Locate and identify every blood parasite.
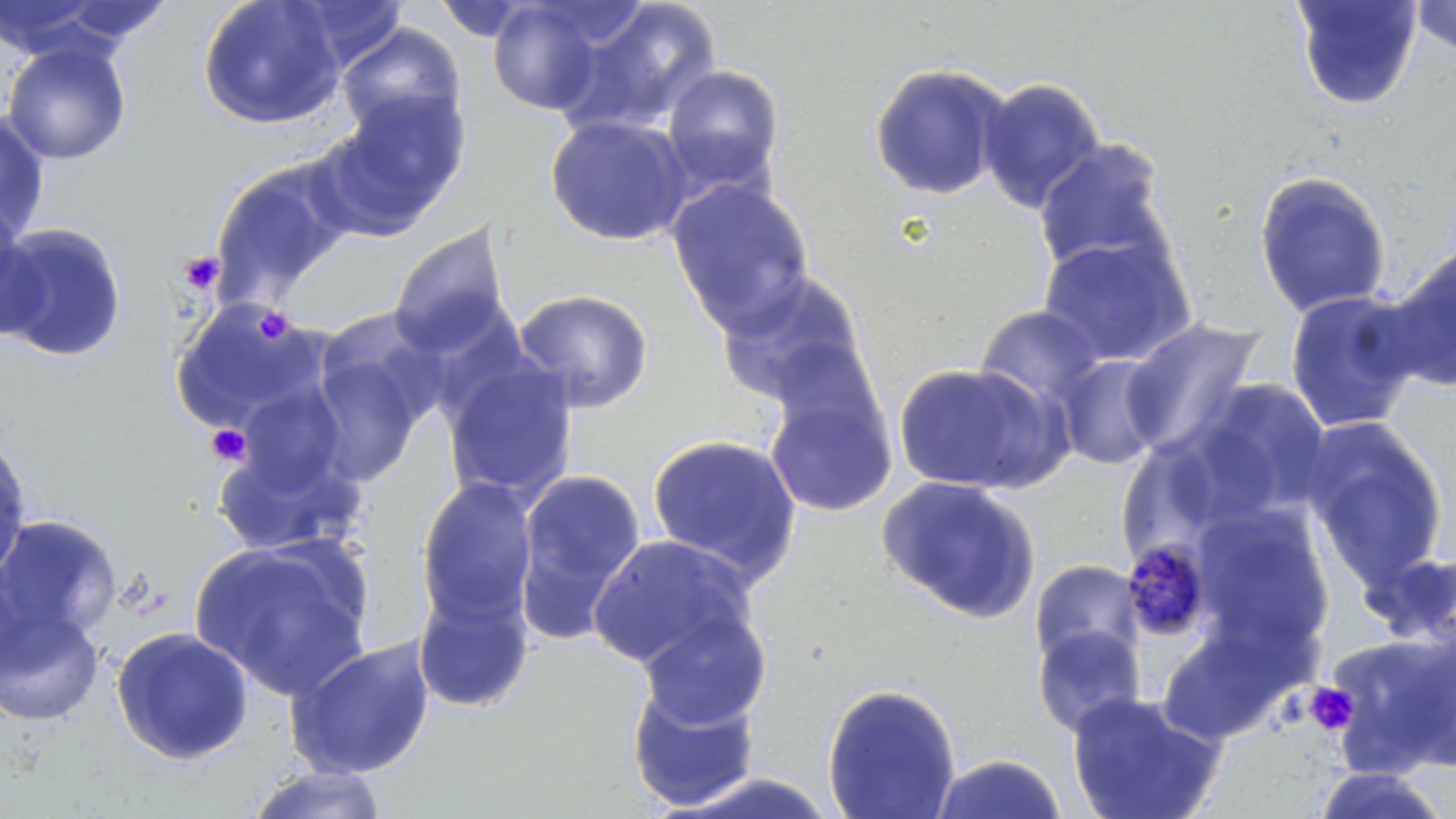
Approximate bounding boxes as [x1, y1, x2, y2] in pixels.
Plasmodium malariae-infected red blood cells: [1118, 533, 1212, 638].
No Plasmodium falciparum, Plasmodium ovale, Plasmodium vivax, Babesia divergens, or Trypanosoma brucei observed.

slide_level_diagnosis: Plasmodium malariae
platelet_locations: 'approximate bounding boxes as [x1, y1, x2, y2] in pixels: [177, 250, 225, 295], [253, 305, 294, 343], [206, 423, 252, 467], [1303, 682, 1359, 736]'
magnification: 1000x
image_size: 1456×819 pixels
preparation: thin blood film
modality: light microscopy
field_of_view: one of a larger specimen
stain: May-Grünwald-Giemsa
uninfected_red_blood_cell_locations: 'approximate bounding boxes as [x1, y1, x2, y2] in pixels: [0, 0, 161, 61], [196, 0, 346, 130], [282, 0, 411, 71], [485, 0, 615, 117], [1409, 0, 1456, 59], [429, 1, 546, 43], [562, 1, 721, 133], [1290, 1, 1423, 111], [336, 22, 467, 141], [1, 40, 132, 165], [868, 62, 1013, 202], [661, 64, 785, 195], [978, 76, 1106, 214], [312, 94, 470, 240], [0, 110, 51, 243], [545, 114, 693, 247], [1033, 138, 1173, 278], [209, 156, 358, 307], [1252, 169, 1392, 319], [665, 177, 816, 334], [0, 205, 44, 342], [1, 222, 128, 363], [387, 222, 515, 359], [1037, 235, 1197, 368], [1380, 244, 1455, 392], [715, 269, 872, 412], [512, 288, 654, 414], [1283, 289, 1423, 434], [169, 297, 327, 434], [975, 304, 1106, 411], [1120, 318, 1267, 460], [308, 333, 432, 488], [1055, 355, 1168, 471], [442, 360, 578, 504], [891, 361, 1064, 495], [1179, 378, 1334, 526], [233, 380, 353, 499], [764, 381, 897, 519], [1301, 417, 1448, 585], [0, 431, 33, 588], [645, 433, 803, 585], [212, 435, 364, 557], [1123, 439, 1212, 558], [513, 469, 647, 641], [877, 475, 1042, 623], [415, 478, 539, 629], [1191, 503, 1336, 656], [0, 514, 121, 642], [586, 534, 758, 675], [188, 537, 374, 701], [1361, 548, 1456, 659], [1029, 559, 1144, 669], [413, 584, 535, 713], [0, 600, 105, 728], [634, 608, 773, 731], [1156, 618, 1306, 745], [1032, 623, 1147, 737], [110, 626, 254, 765], [1326, 631, 1456, 776], [286, 637, 436, 779], [626, 678, 762, 813], [821, 682, 962, 819], [1064, 690, 1227, 819], [929, 753, 1070, 819], [244, 764, 390, 819], [1307, 767, 1454, 818], [658, 770, 843, 818]'